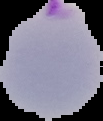
image type = cell region segmented out of the field of view; surrounding area masked to black
image size = 103×121 pixels
result = malaria parasites detected
preparation = thin blood film